Report the malaria status of this cell.
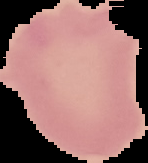

It is uninfected.

From a thin blood smear. The area outside the segmented cell region is set to black. Image is 148×163 pixels.